Locate and identify every blood parasite.
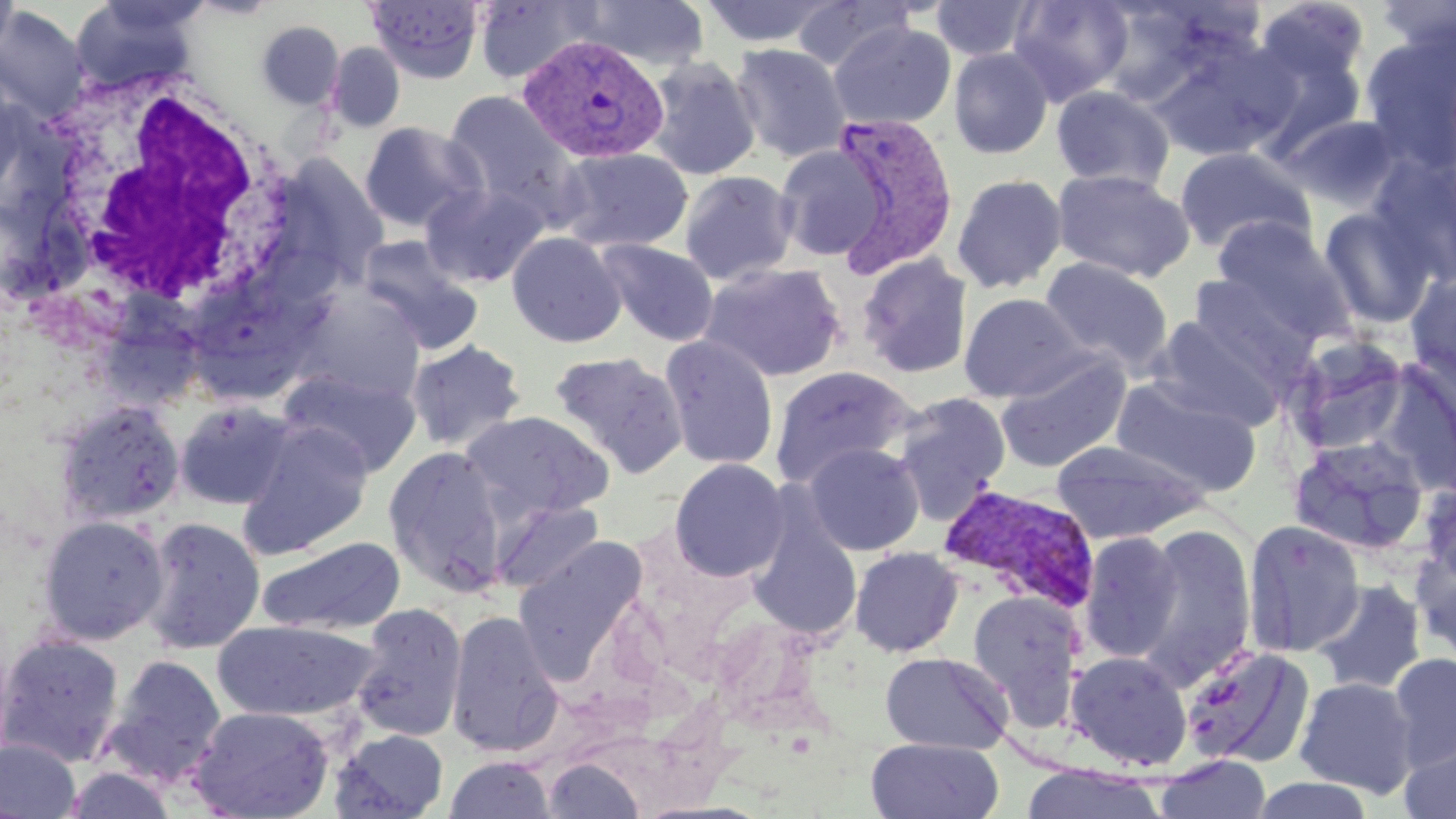

Approximate bounding boxes as (x1, y1, x2, y2) in pixels.
Plasmodium vivax-infected red blood cells: (518, 33, 670, 164), (828, 111, 959, 279), (937, 484, 1101, 614).
No Plasmodium falciparum, Plasmodium ovale, Plasmodium malariae, Babesia divergens, or Trypanosoma brucei observed.

Uninfected red blood cell locations: (0, 0, 18, 65), (69, 0, 206, 93), (365, 0, 485, 84), (473, 0, 601, 83), (578, 0, 709, 70), (698, 0, 841, 48), (1007, 0, 1134, 104), (1376, 0, 1456, 54), (793, 1, 918, 71), (930, 1, 1039, 61), (1258, 1, 1370, 83), (0, 6, 89, 121), (255, 20, 345, 109), (828, 21, 955, 131), (1363, 33, 1455, 174), (1147, 39, 1295, 163), (326, 42, 405, 133), (731, 43, 852, 163), (949, 47, 1054, 160), (644, 56, 761, 181), (1051, 85, 1175, 192), (441, 89, 585, 226), (1284, 115, 1403, 209), (359, 121, 484, 234), (775, 145, 885, 261), (556, 147, 693, 252), (1173, 147, 1315, 255), (269, 153, 389, 293), (1373, 155, 1454, 282), (1051, 169, 1195, 282), (679, 170, 798, 285), (951, 173, 1068, 293), (420, 182, 549, 288), (1320, 207, 1437, 328), (1210, 217, 1351, 338), (506, 231, 627, 348), (357, 235, 484, 354), (597, 239, 718, 346), (856, 254, 973, 379), (1040, 257, 1174, 373), (699, 262, 847, 382), (1406, 273, 1456, 394), (1188, 274, 1317, 381), (289, 287, 426, 403), (958, 293, 1090, 402), (1149, 316, 1287, 432), (659, 335, 779, 470), (1288, 336, 1412, 455), (405, 339, 528, 452), (548, 351, 688, 478), (995, 354, 1131, 473), (1378, 357, 1456, 493), (769, 366, 917, 487), (278, 369, 421, 477), (1110, 378, 1262, 496), (892, 392, 1012, 525), (55, 400, 186, 526), (174, 400, 296, 510), (461, 411, 614, 522), (238, 419, 375, 558), (1288, 436, 1432, 557), (1051, 440, 1208, 545), (803, 442, 925, 555), (383, 446, 508, 595), (669, 458, 790, 581), (1418, 477, 1456, 587), (490, 499, 605, 594), (748, 510, 862, 640), (36, 514, 170, 646), (141, 515, 266, 654), (1242, 519, 1366, 657), (1132, 522, 1257, 687), (1078, 532, 1185, 662), (512, 534, 647, 669), (256, 536, 407, 637), (1412, 542, 1456, 666), (850, 546, 963, 657), (1312, 579, 1426, 695), (967, 590, 1084, 723), (351, 603, 467, 742), (446, 609, 563, 757), (212, 620, 379, 722), (0, 632, 125, 768), (1180, 645, 1315, 769), (1065, 650, 1193, 771), (879, 651, 1013, 754), (1389, 653, 1456, 770), (102, 654, 228, 788), (1295, 676, 1419, 797), (187, 705, 335, 819), (329, 729, 450, 819), (0, 738, 82, 819), (866, 738, 1004, 819), (1398, 740, 1456, 818), (1154, 754, 1272, 819), (443, 756, 555, 818), (542, 756, 646, 818), (1019, 765, 1168, 819), (62, 766, 179, 818), (1251, 776, 1377, 819). White blood cell locations: (26, 67, 305, 322). Slide-level diagnosis: Plasmodium vivax. 1000x magnification. Optical microscopy. May-Grünwald-Giemsa stain. Image is 1456×819 pixels. Single field of view. Thin blood smear.